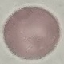
result = negative for malaria parasites
preparation = thin blood smear
stain = Giemsa
image type = automatically extracted cell patch, resized to 64 × 64 pixels
capture = smartphone through the microscope eyepiece